Describe the morphology of the red blood cells.
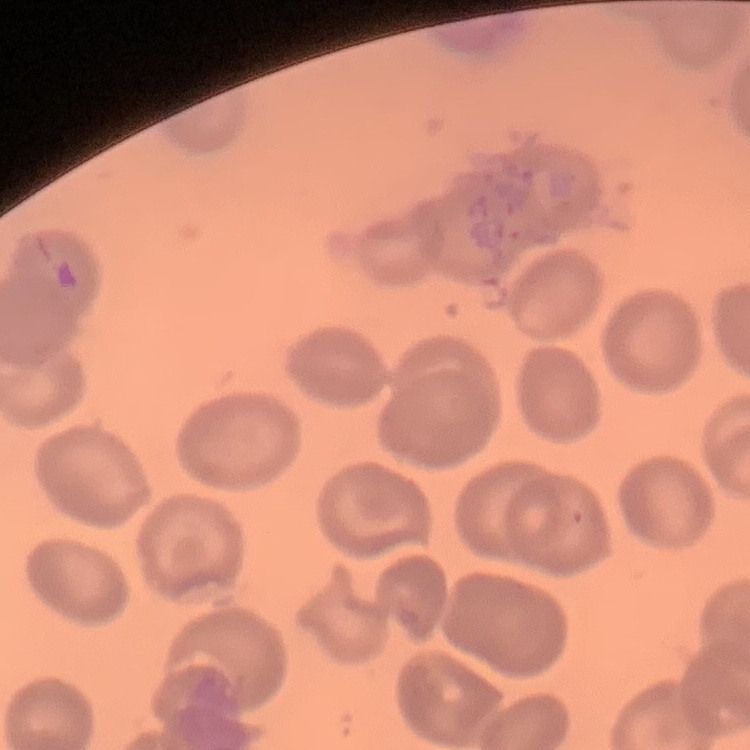
They show no rouleaux formation.

Summary:
  - Stain: Field's or Giemsa
  - Image type: square crop of a larger photomicrograph
  - Preparation: thin blood film